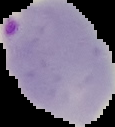
{
  "image_size": "115×127 pixels",
  "preparation": "thin blood smear",
  "result": "Plasmodium parasites identified",
  "image_type": "segmented cell region on a black background"
}